Identify the parasite.
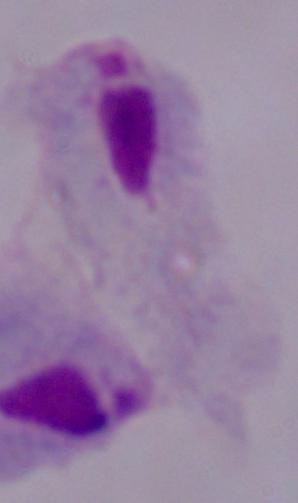

A trichomonad.

1000x magnification. Photomicrograph.